Name the cell type shown.
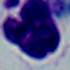
This is a leukocyte.

Summary:
  - Magnification: 1000x
  - Modality: micrograph